Locate every blood parasite and identify its species.
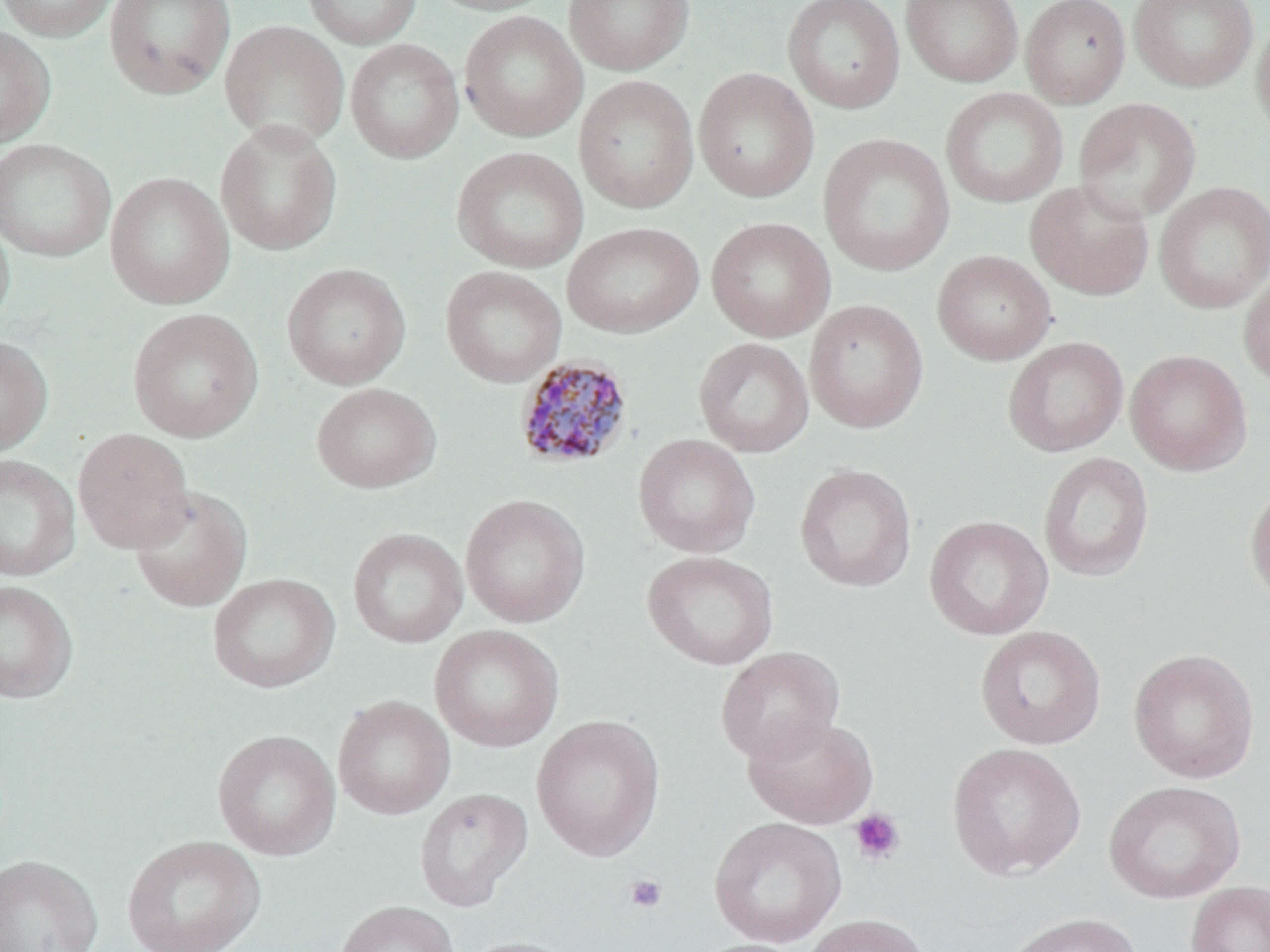
Approximate bounding boxes as (x1,y1)-(x2,y2) corner pairs in pixels.
Plasmodium malariae-infected red blood cells: (513,355)-(635,470).
No Plasmodium falciparum, Plasmodium ovale, Plasmodium vivax, Babesia divergens, or Trypanosoma brucei observed.

slide-level diagnosis = Plasmodium malariae
image size = 1270×952 pixels
modality = light microscopy
field of view = one of a larger specimen
platelet locations = approximate bounding boxes as (x1,y1)-(x2,y2) corner pairs in pixels: (849,808)-(905,865), (624,874)-(667,914)
preparation = thin blood film
uninfected red blood cell locations = approximate bounding boxes as (x1,y1)-(x2,y2) corner pairs in pixels: (0,0)-(120,42), (104,0)-(237,99), (300,0)-(423,49), (422,0)-(557,16), (563,0)-(694,75), (782,0)-(906,114), (900,0)-(1024,87), (1020,0)-(1131,108), (1128,0)-(1258,92), (1252,10)-(1270,143), (459,11)-(587,142), (219,20)-(349,148), (0,25)-(56,148), (345,38)-(464,163), (693,67)-(820,203), (573,75)-(699,213), (940,87)-(1068,208), (1073,97)-(1201,223), (215,119)-(343,256), (817,133)-(955,277), (0,138)-(116,262), (452,146)-(589,273), (105,171)-(235,310), (1025,180)-(1154,300), (1154,181)-(1270,314), (0,210)-(15,331), (706,217)-(836,342), (561,222)-(704,338), (932,250)-(1056,365), (282,263)-(411,389), (440,266)-(567,387), (1238,271)-(1270,387), (804,299)-(928,433), (127,307)-(263,443), (0,335)-(52,457), (1003,336)-(1129,457), (693,337)-(814,458), (1124,349)-(1252,476), (311,382)-(441,493), (73,427)-(193,553), (633,434)-(761,558), (1038,452)-(1154,583), (0,454)-(80,582), (794,463)-(917,592), (1245,480)-(1270,606), (129,485)-(252,612), (460,493)-(591,628), (923,515)-(1053,640), (347,527)-(468,648), (642,550)-(779,671), (208,572)-(339,694), (0,580)-(79,704), (430,624)-(564,752), (975,625)-(1106,749), (715,646)-(845,764), (1128,648)-(1260,783), (333,694)-(455,819), (531,714)-(666,861), (742,714)-(879,829), (212,729)-(341,860), (946,742)-(1086,880), (1103,780)-(1246,903), (414,787)-(533,911), (709,816)-(846,947), (122,834)-(266,952), (0,853)-(104,952), (1185,881)-(1270,952), (335,900)-(459,952), (1003,912)-(1144,952), (803,914)-(931,952), (459,936)-(582,952), (692,938)-(811,952)
stain = May-Grünwald-Giemsa
magnification = 1000x